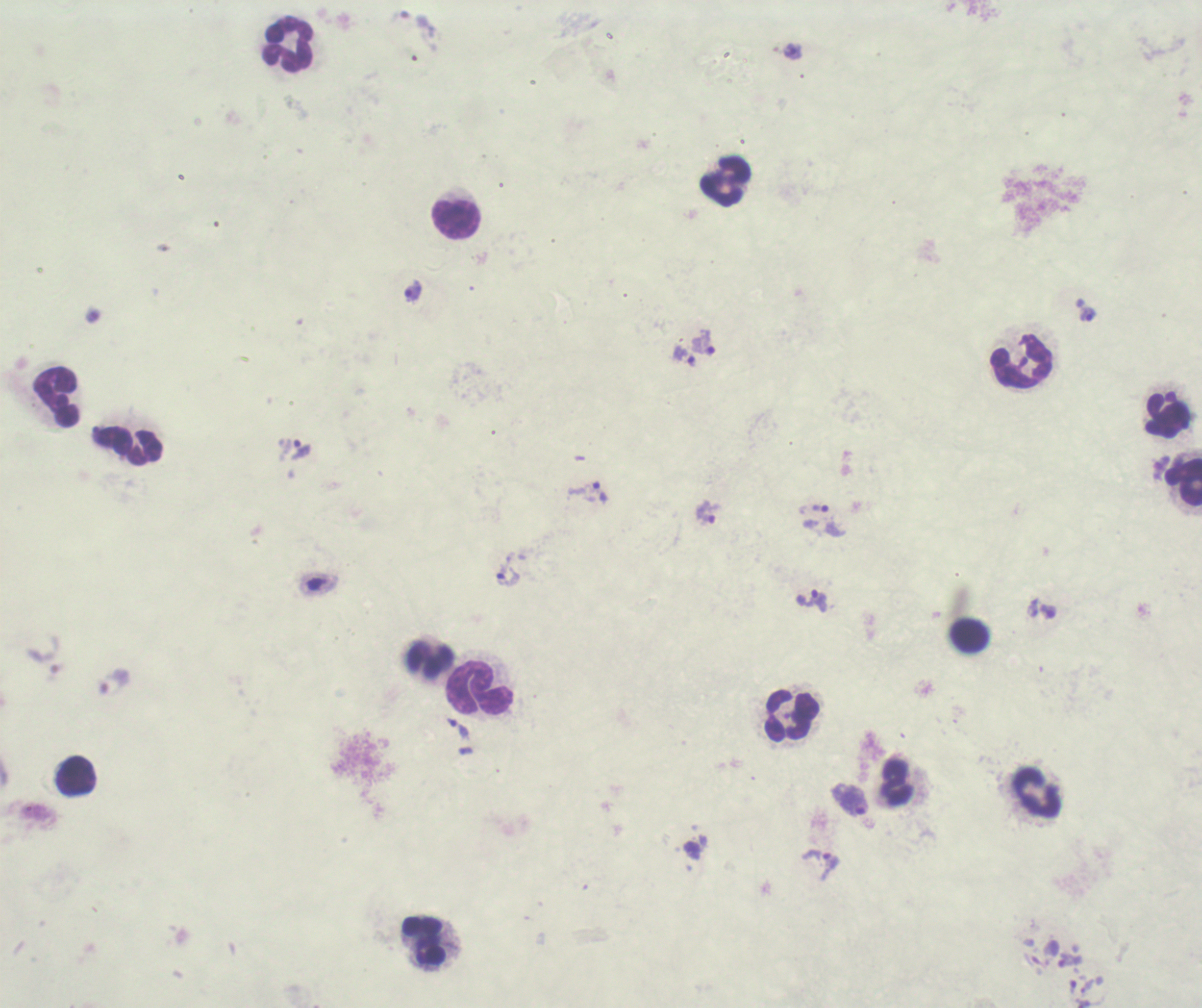

coordinate format = approximate object centers, in pixels from the top-left corner
trophozoite locations = (x=792, y=51), (x=413, y=289), (x=1087, y=315), (x=702, y=342), (x=685, y=356), (x=300, y=449), (x=600, y=491), (x=820, y=508), (x=707, y=511), (x=508, y=574), (x=818, y=600), (x=1048, y=611), (x=115, y=681), (x=460, y=729), (x=852, y=801), (x=829, y=865), (x=1069, y=960), (x=1086, y=986), (x=1072, y=987)
leukocyte locations = (x=288, y=44), (x=726, y=182), (x=456, y=219), (x=1021, y=361), (x=56, y=398), (x=1168, y=415), (x=128, y=445), (x=1184, y=480), (x=970, y=636), (x=428, y=657), (x=480, y=689), (x=792, y=714), (x=76, y=775), (x=897, y=783), (x=1038, y=793), (x=424, y=941)
image size = 1202×1008 pixels
result = positive for Plasmodium parasites
background quality = poor
magnification = 100x
coloration quality = bad
field of view = one from this slide
stain = Romanowsky
preparation = thick blood smear
context = previously used in an actual diagnosis